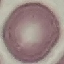
Summary:
  - Result: no malaria parasites detected
  - Image type: automatically extracted cell patch, resized to 64 × 64 pixels
  - Stain: Giemsa
  - Capture: smartphone camera at the microscope eyepiece
  - Preparation: thin blood film